Report the malaria status of this cell.
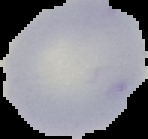
It is uninfected.

Summary:
  - Image type: segmented cell region with the area outside set to black
  - Preparation: thin blood smear
  - Image size: 148×139 pixels